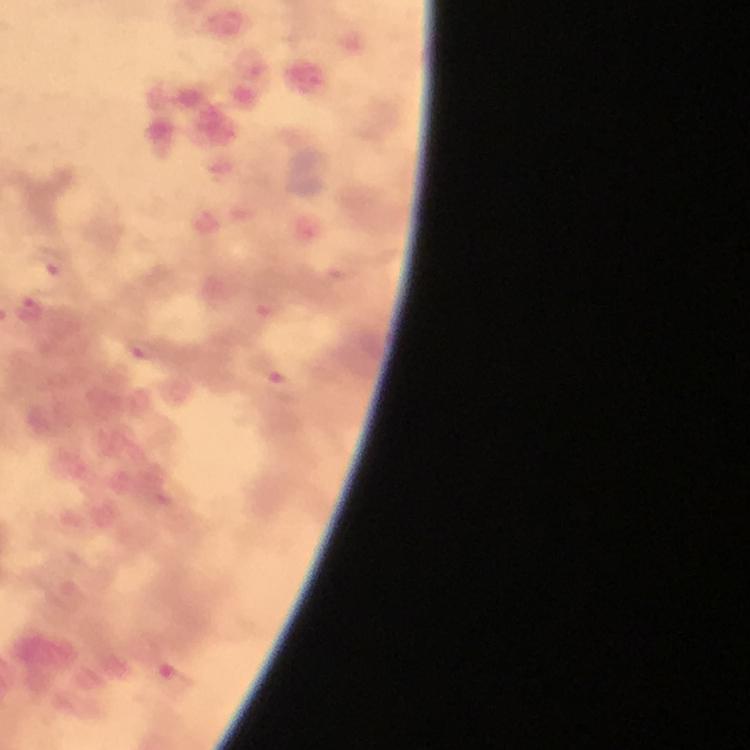
Approximate centers as (x, y) in pixels.
Summary:
  - Plasmodium parasite locations: (53, 261), (26, 310), (139, 349), (268, 369), (175, 679)
  - Immersion oil: applied
  - Image size: 750×750 pixels
  - Magnification: 100x
  - Capture: smartphone photograph through a microscope
  - Stain: Giemsa
  - Context: from a diagnostic examination for malaria
  - Cropped from: a single field of view
  - Preparation: thick blood film